Classify this cell by malaria status.
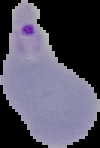

It is parasitized.

Image is 100×148 pixels. From a thin blood smear. Cell region segmented out of the field of view; the surrounding area is masked to black.